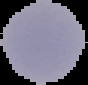 Image is 88×85 pixels. Segmented cell region on a black background. From a thin blood smear. Result: no malaria parasites seen.